Comment on the morphology of the erythrocytes.
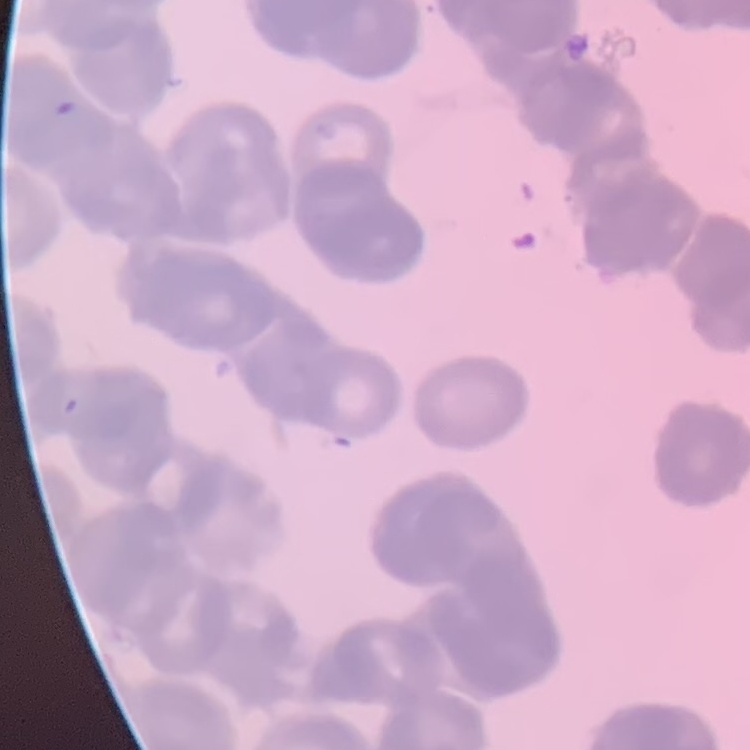
Rouleaux formation.

Square crop of a larger photomicrograph. Stained with either Field's or Giemsa. Thin peripheral smear.